Find the red blood cells and label each as P. falciparum-infected, uninfected, or of indeterminate infection status.
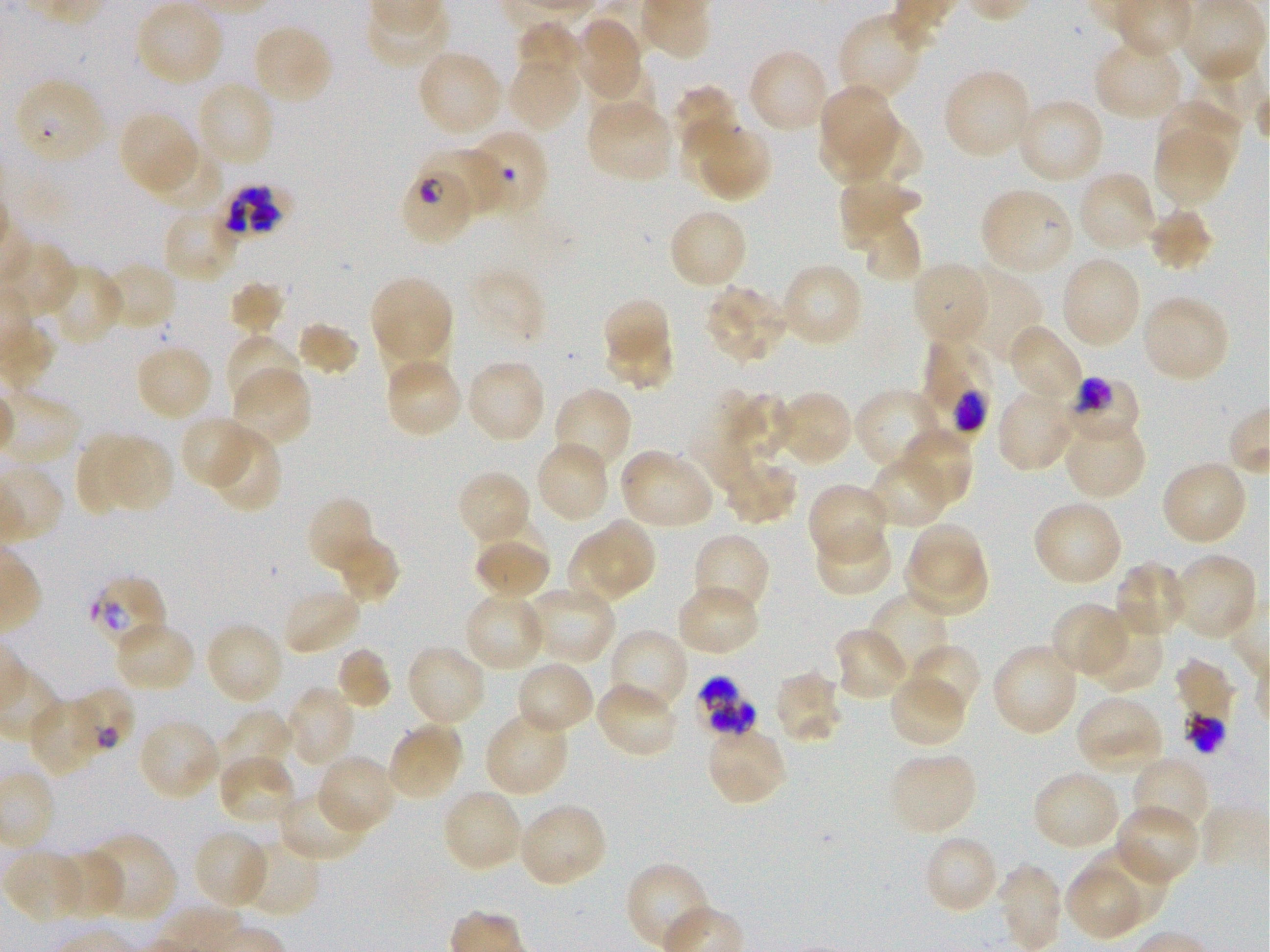

Approximate bounding boxes as {x1, y1, x2, y2} in pixels. Not every red blood cell is marked. A life-cycle stage — or a range of stages, where the recorded stages span more than one — follows each staged infected red blood cell.
Infected red blood cells: {13, 77, 107, 168}; {420, 148, 503, 217}; {401, 172, 469, 245} late ring to early trophozoite; {224, 185, 283, 236}; {922, 334, 996, 441} trophozoite; {1049, 375, 1139, 445} trophozoite; {87, 573, 168, 652}; {692, 678, 757, 738}.
Red blood cells of indeterminate infection status: {64, 689, 135, 762}, {1187, 714, 1227, 755}.
Uninfected red blood cells: {135, 1, 226, 88}, {837, 12, 925, 102}, {572, 16, 644, 102}, {518, 22, 585, 74}, {251, 23, 335, 107}, {1094, 36, 1185, 121}, {746, 48, 832, 135}, {416, 49, 504, 140}, {1193, 52, 1266, 131}, {507, 63, 580, 128}, {586, 64, 657, 132}, {943, 68, 1034, 162}, {194, 80, 276, 169}, {821, 82, 897, 156}, {674, 85, 738, 157}, {1014, 97, 1105, 186}, {586, 100, 676, 185}, {1157, 100, 1243, 180}, {117, 110, 202, 196}, {817, 117, 895, 182}, {847, 118, 923, 187}, {703, 119, 771, 205}, {680, 120, 746, 186}, {477, 128, 549, 213}, {1152, 133, 1229, 203}, {147, 147, 226, 214}, {1077, 170, 1160, 253}, {839, 186, 922, 236}, {979, 186, 1074, 277}, {1148, 205, 1213, 272}, {162, 206, 239, 284}, {667, 206, 748, 291}, {847, 210, 923, 279}, {1058, 255, 1142, 351}, {99, 262, 177, 333}, {779, 262, 864, 348}, {910, 262, 992, 350}, {46, 264, 124, 346}, {959, 268, 1043, 364}, {368, 274, 455, 371}, {229, 280, 287, 336}, {704, 284, 791, 366}, {1140, 294, 1231, 384}, {606, 297, 666, 358}, {295, 322, 359, 378}, {1006, 322, 1085, 408}, {225, 333, 302, 413}, {604, 333, 676, 390}, {134, 343, 214, 423}, {977, 355, 1030, 431}, {383, 356, 463, 440}, {464, 358, 547, 445}, {231, 365, 312, 450}, {695, 385, 766, 492}, {552, 386, 633, 474}, {853, 387, 943, 472}, {996, 388, 1076, 473}, {774, 389, 855, 468}, {1062, 413, 1146, 501}, {179, 415, 258, 490}, {206, 427, 283, 513}, {897, 428, 974, 508}, {110, 433, 174, 511}, {77, 434, 148, 515}, {534, 440, 611, 525}, {618, 447, 715, 530}, {868, 453, 954, 529}, {719, 457, 798, 526}, {1160, 459, 1249, 546}, {455, 469, 533, 547}, {807, 483, 890, 565}, {306, 495, 381, 578}, {1031, 499, 1124, 587}, {594, 518, 659, 591}, {812, 522, 894, 597}, {908, 524, 983, 593}, {472, 532, 551, 602}, {692, 532, 770, 619}, {327, 533, 400, 606}, {565, 535, 633, 601}, {474, 542, 550, 594}, {901, 549, 991, 615}, {1169, 551, 1258, 641}, {1114, 561, 1190, 640}, {675, 582, 761, 658}, {523, 585, 616, 666}, {280, 586, 364, 656}, {870, 589, 952, 677}, {463, 591, 548, 673}, {1050, 602, 1131, 679}, {1082, 617, 1164, 692}, {113, 620, 195, 693}, {205, 621, 285, 706}, {606, 627, 689, 715}, {831, 627, 911, 701}, {404, 643, 488, 728}, {991, 643, 1080, 737}, {906, 644, 982, 720}, {334, 645, 392, 712}, {1175, 658, 1236, 723}, {514, 660, 595, 736}, {773, 669, 844, 745}, {888, 672, 968, 748}, {593, 681, 680, 759}, {284, 686, 357, 768}, {28, 693, 111, 778}, {1074, 694, 1165, 774}, {484, 708, 571, 798}, {215, 710, 295, 787}, {137, 716, 222, 803}, {386, 720, 464, 804}, {705, 726, 787, 806}, {888, 750, 977, 836}, {315, 753, 398, 834}, {217, 754, 298, 828}, {1130, 755, 1210, 839}, {1031, 770, 1123, 852}, {277, 788, 370, 863}, {440, 789, 525, 874}, {516, 802, 608, 889}, {1113, 803, 1199, 886}, {192, 828, 269, 910}, {85, 832, 177, 923}, {922, 833, 1001, 914}, {236, 835, 321, 918}, {1080, 839, 1170, 926}, {2, 849, 86, 925}, {50, 849, 125, 919}, {626, 861, 713, 950}, {995, 863, 1064, 951}, {1064, 871, 1137, 941}.

preparation = thin blood smear
donor blood group = O+
image size = 1270×952 pixels
field of view = single
stain = Giemsa
culture = static in-vitro P. falciparum strain 3D7
objective = 100x, oil immersion, numerical aperture 1.25